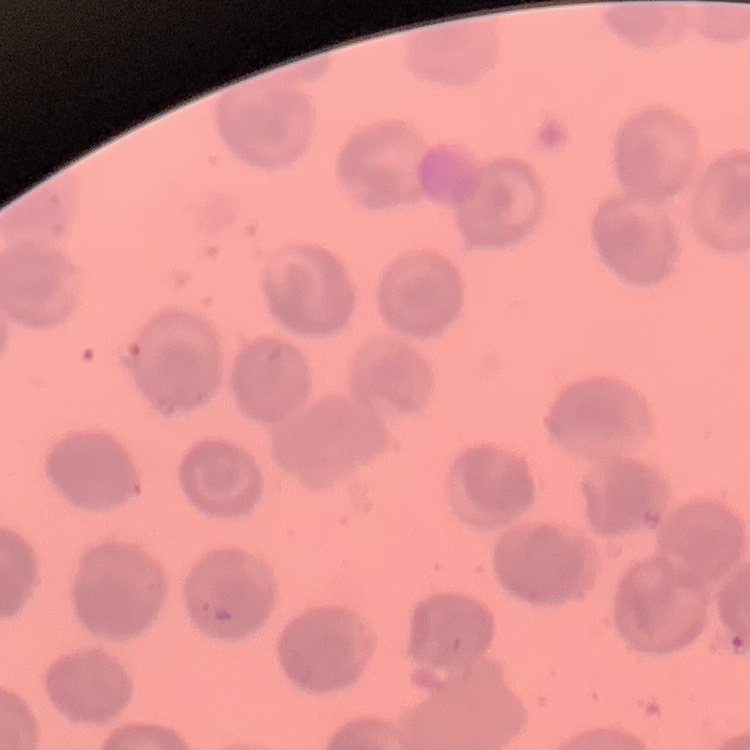 The erythrocytes show no rouleaux formation. Thin blood film. Stained with either Field's or Giemsa. Square crop of a larger photomicrograph.